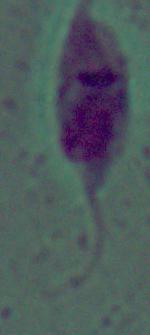

Photomicrograph. A Leishmania parasite is seen. 1000x magnification.